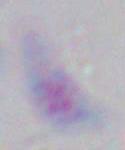 Toxoplasma gondii is seen. Photomicrograph. Captured at 1000x magnification.